Classify this cell by malaria status.
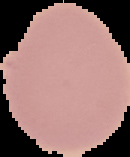

Uninfected.

{
  "image_type": "cell region segmented out of the field of view; surrounding area masked to black",
  "image_size": "130×157 pixels",
  "preparation": "thin blood smear"
}